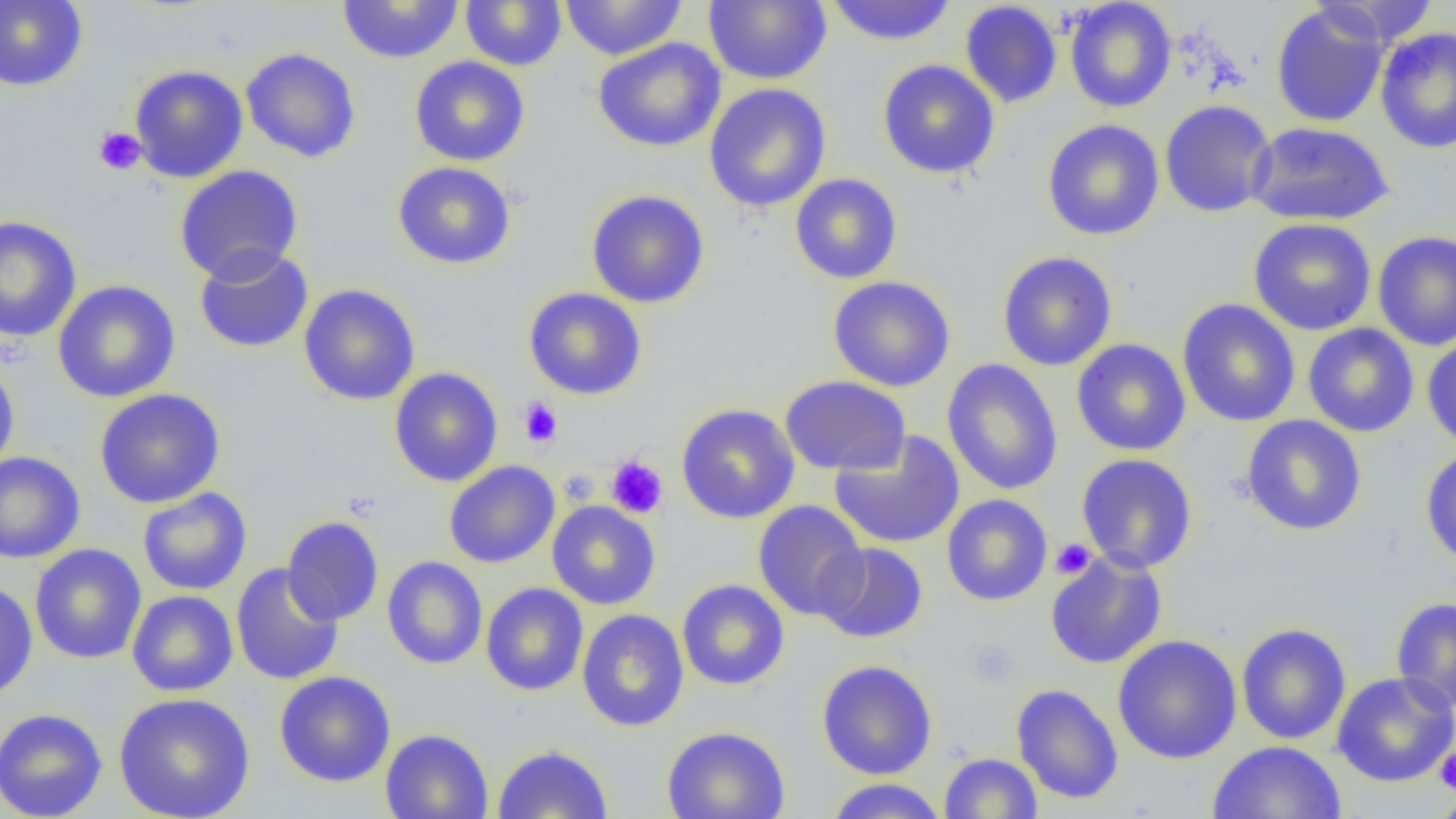

slide-level diagnosis = no evidence of blood parasites
image size = 1456×819 pixels
platelet locations = approximate bounding boxes as (x1, y1, x2, y2) in pixels: (93, 127, 146, 176), (518, 396, 563, 447), (606, 455, 668, 518), (559, 469, 599, 507), (1051, 539, 1095, 579), (965, 639, 1020, 688), (1434, 747, 1456, 796), (1431, 792, 1456, 818)
field of view = single
preparation = thin blood film
modality = optical microscopy
magnification = 1000x
uninfected red blood cell locations = approximate bounding boxes as (x1, y1, x2, y2) in pixels: (0, 0, 88, 91), (460, 0, 567, 72), (559, 0, 687, 60), (703, 0, 831, 85), (824, 0, 957, 46), (1064, 0, 1177, 112), (1311, 0, 1440, 48), (337, 1, 464, 64), (959, 2, 1062, 108), (1271, 4, 1389, 127), (1375, 27, 1456, 154), (592, 37, 726, 153), (240, 47, 362, 163), (409, 56, 530, 166), (877, 59, 1000, 179), (129, 64, 248, 183), (704, 83, 831, 213), (1159, 99, 1276, 218), (1042, 119, 1164, 241), (1246, 121, 1394, 226), (392, 161, 516, 269), (174, 164, 304, 284), (790, 173, 903, 284), (586, 189, 710, 308), (0, 215, 82, 343), (1248, 217, 1377, 336), (1372, 230, 1456, 352), (194, 246, 313, 354), (997, 251, 1118, 371), (828, 275, 956, 392), (53, 280, 181, 403), (298, 284, 421, 406), (523, 287, 647, 400), (1176, 299, 1301, 427), (1303, 323, 1419, 437), (1422, 334, 1456, 451), (1071, 338, 1191, 456), (0, 358, 20, 476), (941, 358, 1063, 495), (389, 367, 503, 487), (779, 376, 910, 475), (94, 388, 226, 508), (676, 403, 800, 524), (1240, 415, 1367, 536), (829, 431, 965, 549), (1420, 445, 1456, 569), (0, 452, 85, 563), (1075, 453, 1198, 573), (444, 460, 560, 568), (137, 487, 252, 596), (941, 494, 1053, 606), (752, 500, 868, 621), (547, 501, 660, 610), (281, 516, 384, 625), (815, 543, 928, 642), (29, 544, 146, 664), (1045, 551, 1167, 669), (382, 556, 488, 670), (231, 562, 344, 685), (676, 579, 790, 690), (0, 580, 37, 703), (481, 582, 589, 696), (126, 590, 238, 696), (1390, 596, 1456, 713), (576, 609, 689, 732), (1236, 622, 1351, 745), (1112, 634, 1242, 764), (816, 660, 937, 780), (274, 671, 396, 788), (1332, 671, 1456, 788), (1011, 683, 1124, 805), (113, 692, 255, 819), (0, 707, 108, 819), (661, 725, 791, 819), (378, 729, 494, 819), (1208, 740, 1347, 818), (492, 744, 613, 819), (939, 752, 1043, 818), (823, 778, 949, 819), (1430, 792, 1456, 819)